Report the malaria status of this cell.
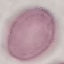
Uninfected.

Summary:
  - Preparation: thin blood smear
  - Image type: automatically extracted cell patch, resized to 64 × 64 pixels
  - Capture: smartphone through the microscope eyepiece
  - Stain: Giemsa